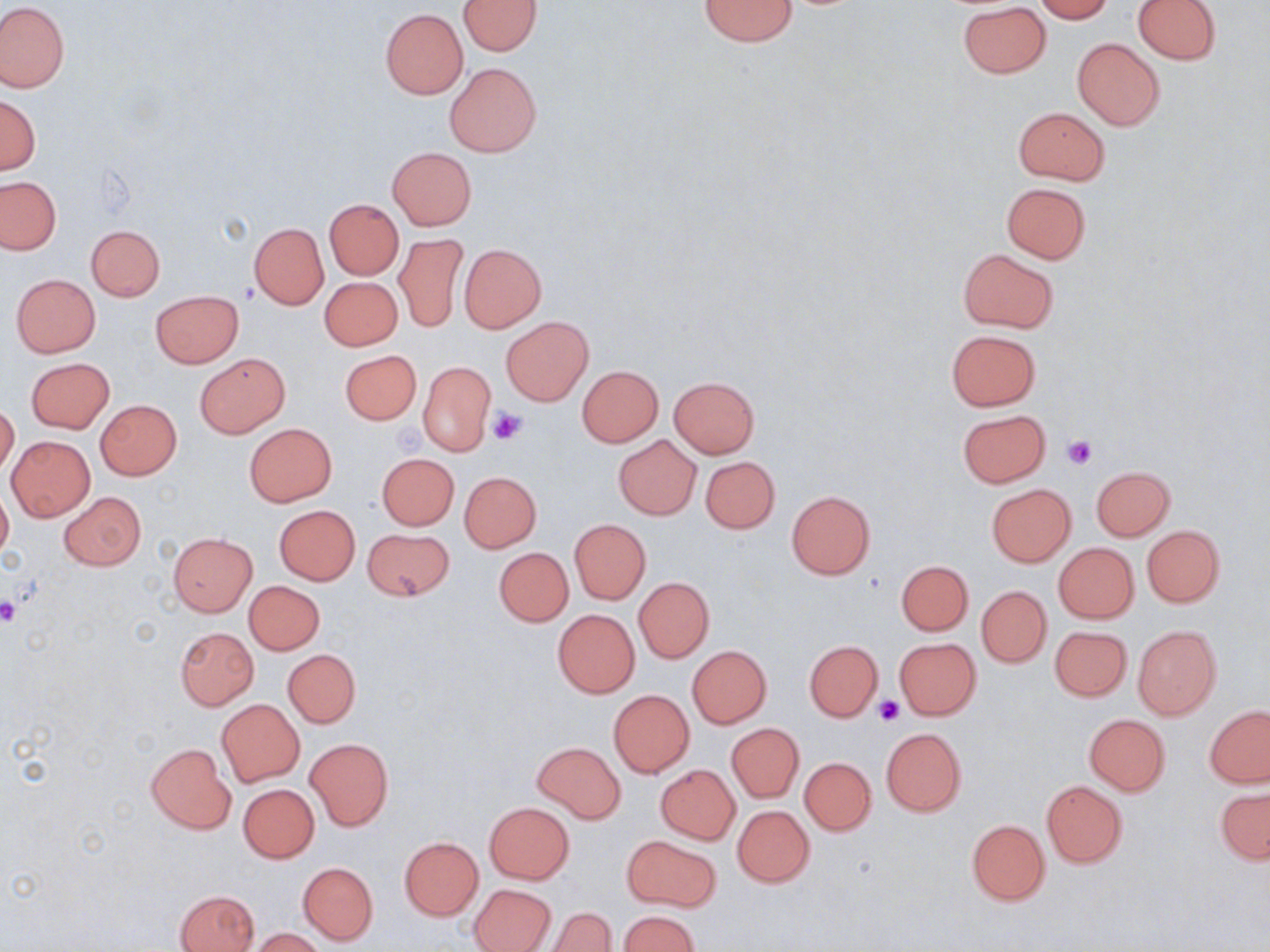

Approximate bounding boxes as named x1/y1/x2/y2 corners in pixels. Uninfected red blood cell locations: (x1=699, y1=0, x2=796, y2=46), (x1=1033, y1=0, x2=1115, y2=22), (x1=1132, y1=0, x2=1220, y2=65), (x1=458, y1=1, x2=542, y2=55), (x1=0, y1=3, x2=69, y2=92), (x1=957, y1=3, x2=1051, y2=78), (x1=380, y1=8, x2=468, y2=99), (x1=1072, y1=38, x2=1164, y2=130), (x1=446, y1=62, x2=542, y2=157), (x1=0, y1=94, x2=40, y2=174), (x1=1013, y1=107, x2=1110, y2=184), (x1=388, y1=148, x2=476, y2=230), (x1=0, y1=177, x2=61, y2=254), (x1=1001, y1=183, x2=1092, y2=263), (x1=325, y1=199, x2=403, y2=279), (x1=249, y1=223, x2=328, y2=309), (x1=86, y1=225, x2=165, y2=300), (x1=394, y1=234, x2=467, y2=333), (x1=460, y1=244, x2=547, y2=333), (x1=957, y1=248, x2=1059, y2=333), (x1=11, y1=273, x2=101, y2=357), (x1=320, y1=277, x2=402, y2=351), (x1=151, y1=291, x2=243, y2=368), (x1=501, y1=317, x2=593, y2=406), (x1=946, y1=329, x2=1040, y2=410), (x1=340, y1=350, x2=422, y2=425), (x1=195, y1=354, x2=289, y2=437), (x1=26, y1=358, x2=114, y2=433), (x1=418, y1=361, x2=494, y2=455), (x1=577, y1=366, x2=664, y2=448), (x1=669, y1=376, x2=760, y2=457), (x1=96, y1=400, x2=181, y2=479), (x1=0, y1=403, x2=19, y2=477), (x1=957, y1=409, x2=1051, y2=487), (x1=244, y1=423, x2=337, y2=506), (x1=613, y1=434, x2=701, y2=519), (x1=6, y1=435, x2=95, y2=521), (x1=376, y1=453, x2=459, y2=530), (x1=701, y1=456, x2=780, y2=534), (x1=1089, y1=465, x2=1174, y2=540), (x1=460, y1=471, x2=541, y2=552), (x1=987, y1=484, x2=1076, y2=566), (x1=0, y1=488, x2=12, y2=560), (x1=786, y1=490, x2=875, y2=579), (x1=59, y1=491, x2=146, y2=570), (x1=274, y1=505, x2=360, y2=586), (x1=569, y1=519, x2=650, y2=604), (x1=1141, y1=526, x2=1224, y2=608), (x1=362, y1=528, x2=456, y2=601), (x1=168, y1=533, x2=257, y2=615), (x1=1054, y1=543, x2=1139, y2=623), (x1=495, y1=548, x2=573, y2=626), (x1=895, y1=560, x2=973, y2=635), (x1=634, y1=577, x2=713, y2=662), (x1=245, y1=581, x2=325, y2=654), (x1=978, y1=586, x2=1050, y2=667), (x1=552, y1=610, x2=639, y2=698), (x1=1132, y1=625, x2=1221, y2=721), (x1=1050, y1=626, x2=1131, y2=701), (x1=176, y1=627, x2=258, y2=710), (x1=893, y1=638, x2=982, y2=720), (x1=805, y1=640, x2=882, y2=721), (x1=687, y1=645, x2=771, y2=727), (x1=284, y1=649, x2=360, y2=727), (x1=609, y1=690, x2=694, y2=777), (x1=217, y1=699, x2=304, y2=786), (x1=1205, y1=706, x2=1270, y2=788), (x1=1084, y1=714, x2=1171, y2=795), (x1=728, y1=723, x2=803, y2=802), (x1=881, y1=728, x2=966, y2=816), (x1=305, y1=738, x2=393, y2=832), (x1=533, y1=742, x2=624, y2=823), (x1=146, y1=743, x2=237, y2=834), (x1=800, y1=757, x2=875, y2=835), (x1=656, y1=765, x2=741, y2=843), (x1=1042, y1=781, x2=1127, y2=867), (x1=238, y1=784, x2=319, y2=862), (x1=1215, y1=787, x2=1269, y2=864), (x1=484, y1=802, x2=574, y2=884), (x1=733, y1=805, x2=814, y2=887), (x1=966, y1=819, x2=1050, y2=904), (x1=623, y1=835, x2=719, y2=912), (x1=399, y1=837, x2=483, y2=920), (x1=298, y1=862, x2=378, y2=945), (x1=471, y1=884, x2=555, y2=951), (x1=175, y1=890, x2=258, y2=952), (x1=545, y1=907, x2=616, y2=952), (x1=620, y1=911, x2=699, y2=952), (x1=251, y1=928, x2=325, y2=952). Platelet locations: (x1=487, y1=406, x2=528, y2=444), (x1=1063, y1=436, x2=1097, y2=470), (x1=0, y1=600, x2=21, y2=626), (x1=873, y1=695, x2=903, y2=724). Slide-level diagnosis: no evidence of blood parasites. Light microscopy. May-Grünwald-Giemsa-stained preparation. Image is 1270×952 pixels. Captured at 1000x magnification. One field of a larger specimen. Thin blood film.